Assess this cell for malaria.
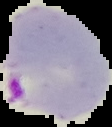

It is parasitized.

Summary:
  - Preparation: thin blood smear
  - Image type: segmented cell region with the area outside set to black
  - Image size: 112×127 pixels